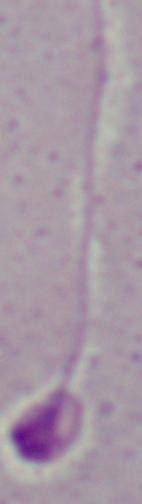

Summary:
  - Modality: micrograph
  - Identification: Leishmania
  - Magnification: 1000x